Name the blood parasite species.
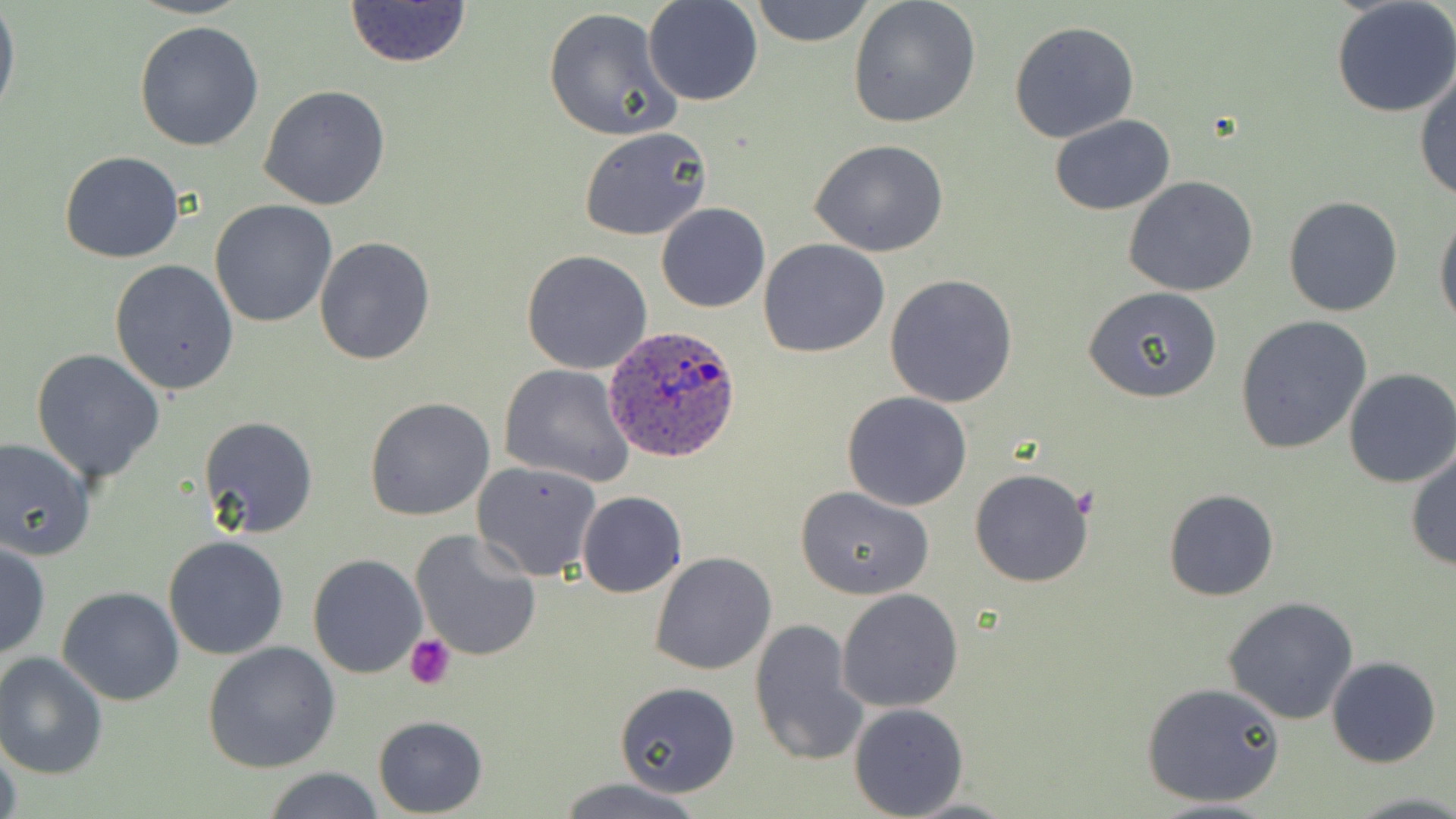
Plasmodium ovale.

{
  "magnification": "1000x",
  "stain": "May-Grünwald-Giemsa",
  "platelet_locations": "approximate bounding boxes as named x1/y1/x2/y2 corners in pixels: (x1=405, y1=634, x2=455, y2=687)",
  "modality": "light microscopy",
  "preparation": "thin blood smear",
  "image_size": "1456×819 pixels",
  "uninfected_red_blood_cell_locations": "approximate bounding boxes as named x1/y1/x2/y2 corners in pixels: (x1=643, y1=0, x2=762, y2=105), (x1=749, y1=0, x2=875, y2=47), (x1=1331, y1=0, x2=1456, y2=117), (x1=342, y1=1, x2=473, y2=69), (x1=848, y1=1, x2=982, y2=129), (x1=0, y1=7, x2=20, y2=121), (x1=543, y1=7, x2=683, y2=144), (x1=134, y1=19, x2=266, y2=152), (x1=1009, y1=21, x2=1139, y2=142), (x1=1413, y1=66, x2=1456, y2=202), (x1=258, y1=85, x2=391, y2=211), (x1=1050, y1=114, x2=1176, y2=216), (x1=579, y1=126, x2=713, y2=241), (x1=810, y1=139, x2=951, y2=257), (x1=59, y1=151, x2=186, y2=262), (x1=1124, y1=175, x2=1259, y2=297), (x1=1282, y1=195, x2=1402, y2=318), (x1=210, y1=200, x2=336, y2=327), (x1=656, y1=202, x2=770, y2=314), (x1=1435, y1=213, x2=1456, y2=334), (x1=313, y1=237, x2=436, y2=365), (x1=758, y1=238, x2=889, y2=357), (x1=521, y1=251, x2=653, y2=374), (x1=109, y1=259, x2=239, y2=396), (x1=884, y1=274, x2=1018, y2=408), (x1=1083, y1=285, x2=1222, y2=404), (x1=1234, y1=316, x2=1371, y2=453), (x1=31, y1=348, x2=164, y2=484), (x1=499, y1=363, x2=636, y2=487), (x1=1343, y1=368, x2=1456, y2=488), (x1=841, y1=392, x2=973, y2=512), (x1=364, y1=397, x2=497, y2=521), (x1=198, y1=415, x2=318, y2=538), (x1=0, y1=435, x2=96, y2=559), (x1=1405, y1=449, x2=1455, y2=570), (x1=470, y1=460, x2=603, y2=580), (x1=969, y1=467, x2=1095, y2=587), (x1=794, y1=487, x2=934, y2=600), (x1=1162, y1=489, x2=1280, y2=602), (x1=576, y1=491, x2=687, y2=597), (x1=410, y1=528, x2=544, y2=663), (x1=163, y1=535, x2=289, y2=659), (x1=0, y1=540, x2=50, y2=660), (x1=650, y1=552, x2=777, y2=675), (x1=308, y1=554, x2=427, y2=678), (x1=57, y1=586, x2=185, y2=706), (x1=837, y1=589, x2=964, y2=712), (x1=1224, y1=597, x2=1359, y2=723), (x1=750, y1=618, x2=869, y2=767), (x1=202, y1=639, x2=341, y2=773), (x1=0, y1=653, x2=108, y2=779), (x1=1327, y1=657, x2=1440, y2=768), (x1=1141, y1=681, x2=1286, y2=809), (x1=614, y1=682, x2=742, y2=796), (x1=848, y1=701, x2=969, y2=818), (x1=371, y1=715, x2=488, y2=816), (x1=0, y1=738, x2=21, y2=819), (x1=264, y1=767, x2=385, y2=819), (x1=555, y1=777, x2=705, y2=819), (x1=1142, y1=798, x2=1284, y2=819)",
  "plasmodium_ovale_infected_red_blood_cell_locations": "approximate bounding boxes as named x1/y1/x2/y2 corners in pixels: (x1=604, y1=325, x2=742, y2=464)",
  "field_of_view": "single"
}